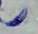
Toxoplasma gondii is seen. 1000x magnification. Micrograph.